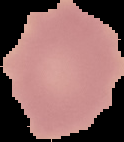
Malaria status: uninfected. Segmented cell region on a black background. From a thin blood smear. Image is 124×142 pixels.